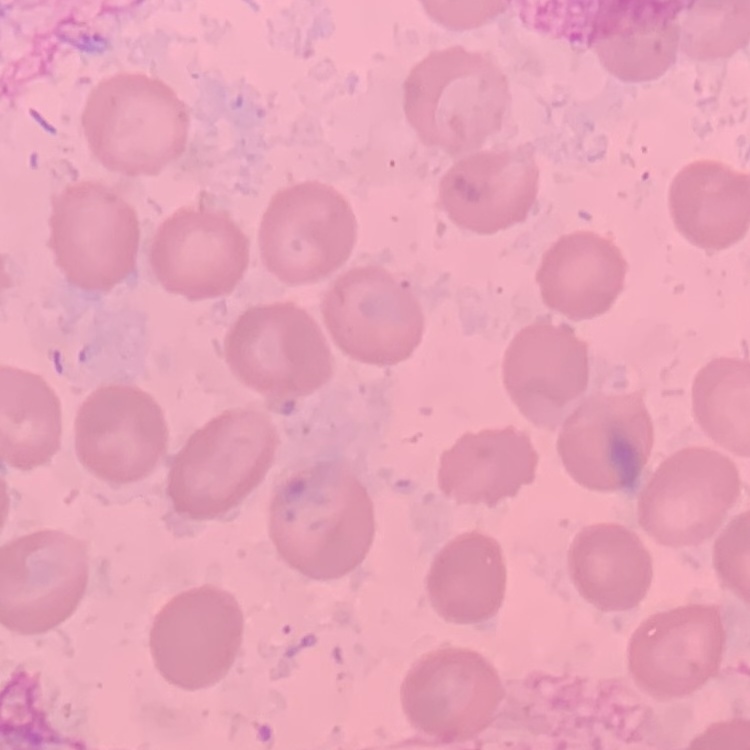

Summary:
  - Erythrocyte morphology: no rouleaux formation
  - Stain: Field's or Giemsa
  - Image type: square crop of a larger photomicrograph
  - Preparation: thin peripheral smear